Name the parasite shown.
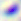

This is Toxoplasma gondii.

Summary:
  - Magnification: 400x
  - Modality: photomicrograph